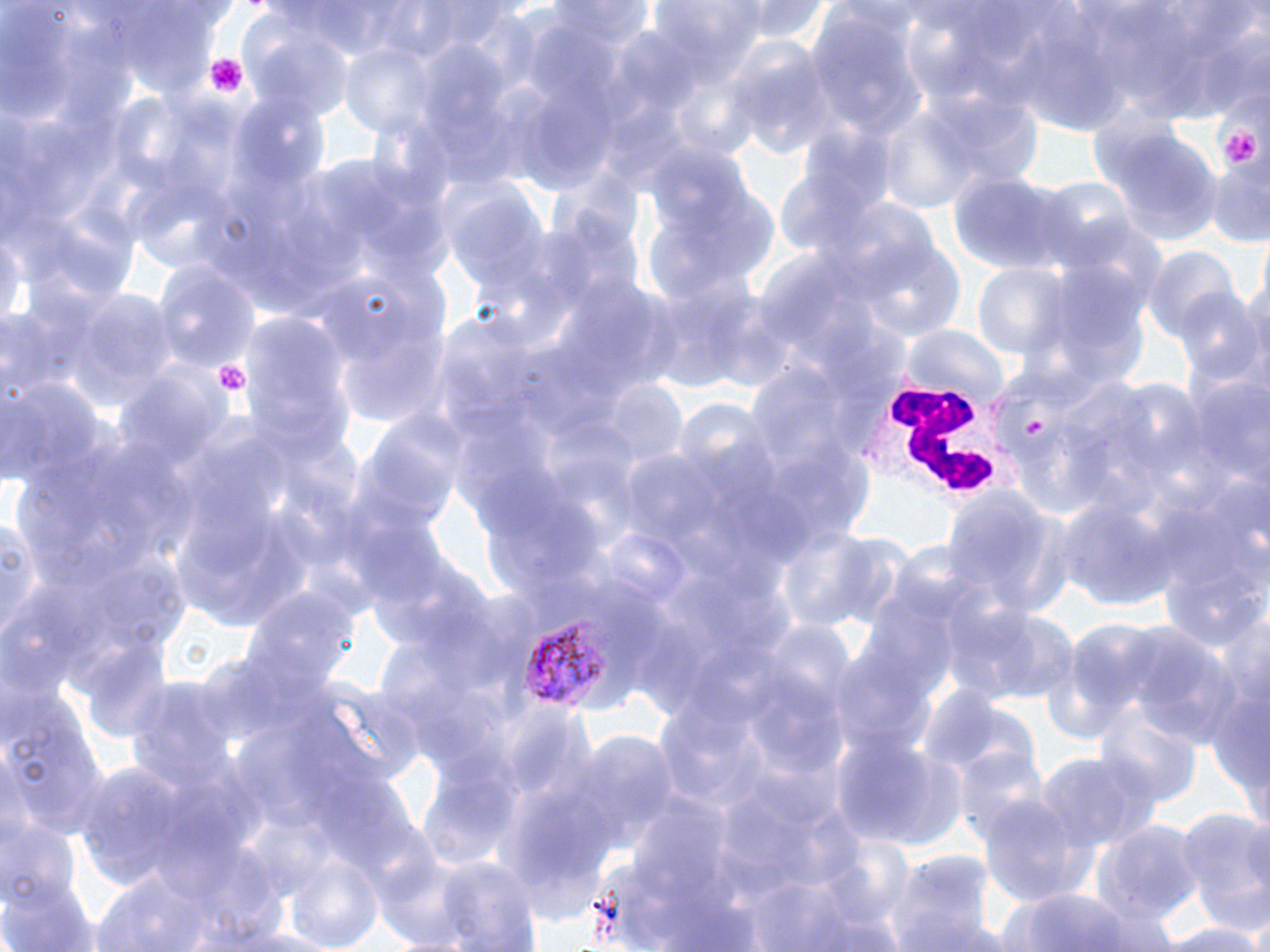

{
  "slide_level_diagnosis": "Plasmodium vivax",
  "field_of_view": "single",
  "preparation": "thin blood film",
  "plasmodium_vivax_infected_red_blood_cell_locations": "approximate bounding boxes as (x1, y1, x2, y2) in pixels: (519, 616, 615, 710)",
  "uninfected_red_blood_cell_locations": "approximate bounding boxes as (x1, y1, x2, y2) in pixels: (739, 0, 834, 46), (1013, 12, 1133, 134), (803, 14, 924, 149), (245, 24, 354, 122), (338, 42, 444, 139), (733, 51, 840, 160), (923, 89, 1042, 191), (876, 113, 981, 216), (1105, 134, 1222, 243), (1206, 160, 1268, 248), (947, 170, 1082, 278), (438, 178, 545, 296), (857, 244, 967, 342), (1143, 248, 1236, 345), (154, 262, 256, 372), (971, 263, 1074, 363), (69, 290, 176, 402), (1173, 290, 1265, 392), (240, 309, 354, 459), (900, 323, 1007, 410), (749, 362, 881, 483), (0, 372, 103, 490), (1186, 381, 1270, 490), (602, 382, 689, 468), (939, 488, 1071, 619), (1052, 491, 1183, 612), (3, 513, 43, 649), (1159, 538, 1270, 656), (239, 584, 360, 701), (945, 600, 1080, 705), (1128, 627, 1245, 751), (2, 690, 110, 840), (1096, 707, 1199, 810), (567, 730, 682, 842), (835, 730, 967, 849), (952, 745, 1050, 846), (1035, 749, 1156, 853), (976, 794, 1090, 909), (1174, 804, 1270, 936), (0, 815, 80, 910), (1094, 817, 1203, 926), (886, 848, 997, 952), (289, 851, 383, 952), (389, 852, 546, 948), (86, 870, 225, 952), (1, 873, 100, 952), (1004, 884, 1140, 952), (1079, 901, 1187, 952), (1241, 906, 1270, 952), (1159, 921, 1270, 952)",
  "platelet_locations": "approximate bounding boxes as (x1, y1, x2, y2) in pixels: (205, 53, 247, 96), (1206, 100, 1267, 182), (210, 357, 251, 398)",
  "stain": "May-Grünwald-Giemsa",
  "image_size": "1270×952 pixels",
  "magnification": "1000x",
  "modality": "light microscopy",
  "white_blood_cell_locations": "approximate bounding boxes as (x1, y1, x2, y2) in pixels: (855, 372, 1035, 507)"
}